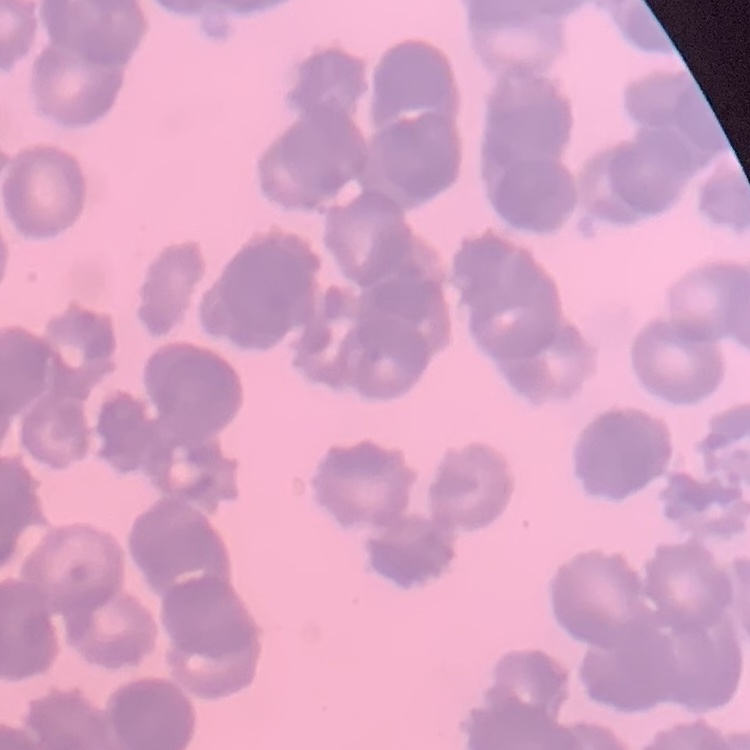
red blood cell morphology = rouleaux formation
stain = Field's or Giemsa
image type = one tile cut from a larger photomicrograph
preparation = thin blood film